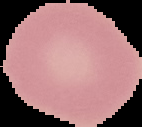
image size = 142×127 pixels
preparation = thin blood film
image type = segmented cell region with the area outside set to black
result = no Plasmodium parasites seen